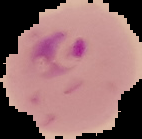 From a thin blood smear. Image is 142×139 pixels. Segmented cell region on a black background. Result: Plasmodium parasites identified.